Name the blood parasite species.
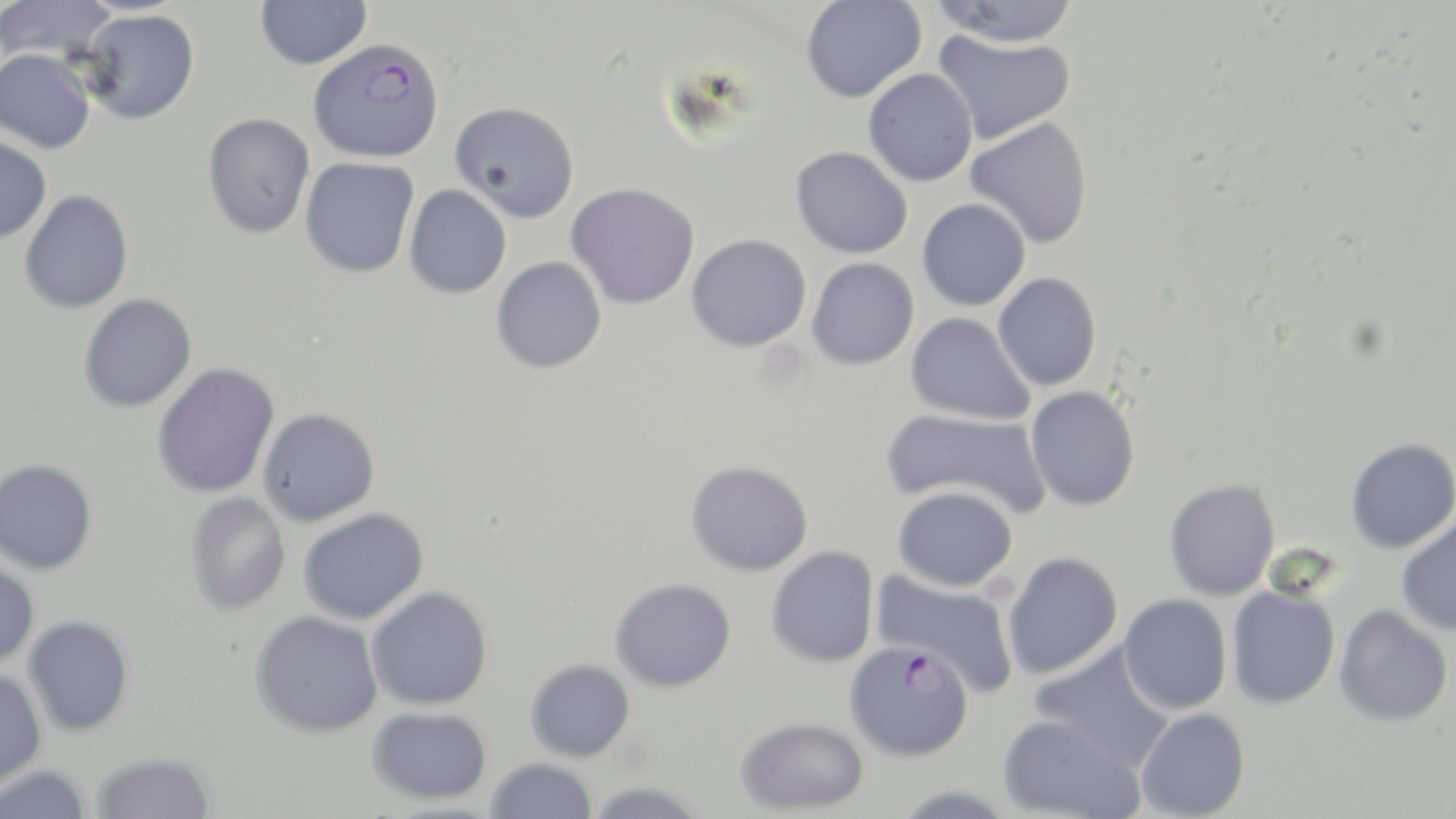
Plasmodium falciparum.

field_of_view: one of a larger specimen
image_size: 1456×819 pixels
magnification: 1000x
stain: May-Grünwald-Giemsa
uninfected_red_blood_cell_locations: 'approximate bounding boxes as (x1, y1, x2, y2) in pixels: (0, 0, 117, 62), (255, 0, 372, 70), (801, 0, 927, 103), (931, 0, 1081, 48), (80, 9, 199, 124), (932, 29, 1076, 145), (0, 48, 95, 153), (863, 68, 977, 187), (450, 101, 579, 222), (202, 113, 315, 238), (965, 117, 1093, 249), (0, 135, 51, 244), (791, 146, 912, 259), (300, 157, 419, 278), (566, 182, 699, 308), (404, 185, 512, 298), (20, 190, 133, 313), (917, 198, 1030, 311), (687, 234, 811, 352), (491, 256, 607, 373), (807, 257, 919, 370), (993, 273, 1101, 391), (79, 294, 196, 413), (906, 312, 1035, 425), (153, 363, 280, 498), (1025, 386, 1140, 511), (258, 408, 380, 526), (881, 408, 1051, 518), (1345, 438, 1456, 553), (0, 458, 98, 574), (685, 460, 814, 576), (1164, 479, 1280, 601), (892, 485, 1018, 591), (185, 493, 290, 615), (299, 508, 429, 625), (1396, 513, 1456, 636), (766, 545, 880, 668), (1002, 551, 1123, 679), (0, 559, 39, 667), (871, 570, 1019, 694), (610, 577, 736, 692), (1226, 585, 1341, 708), (366, 586, 493, 710), (1119, 594, 1233, 714), (1334, 605, 1453, 726), (250, 611, 384, 738), (23, 615, 135, 737), (1030, 644, 1177, 771), (525, 659, 635, 762), (0, 669, 47, 790), (367, 707, 492, 804), (1135, 707, 1251, 818), (997, 714, 1146, 819), (735, 716, 869, 815), (90, 752, 216, 818), (484, 757, 598, 819), (0, 764, 93, 818), (582, 781, 710, 818)'
modality: light microscopy
preparation: thin blood smear
plasmodium_falciparum_infected_red_blood_cell_locations: 'approximate bounding boxes as (x1, y1, x2, y2) in pixels: (308, 37, 444, 162), (844, 640, 974, 761)'